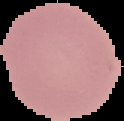

preparation = thin blood smear
image size = 124×121 pixels
result = negative for malaria parasites
image type = segmented cell region with the area outside set to black